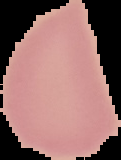

Summary:
  - Image type: segmented cell region on a black background
  - Image size: 121×160 pixels
  - Preparation: thin blood smear
  - Result: negative for Plasmodium parasites